Report the malaria status of this cell.
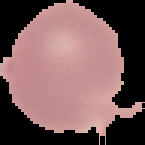
It is uninfected.

Summary:
  - Image type: segmented cell region with the area outside set to black
  - Image size: 145×145 pixels
  - Preparation: thin blood smear